Comment on the morphology of the red blood cells.
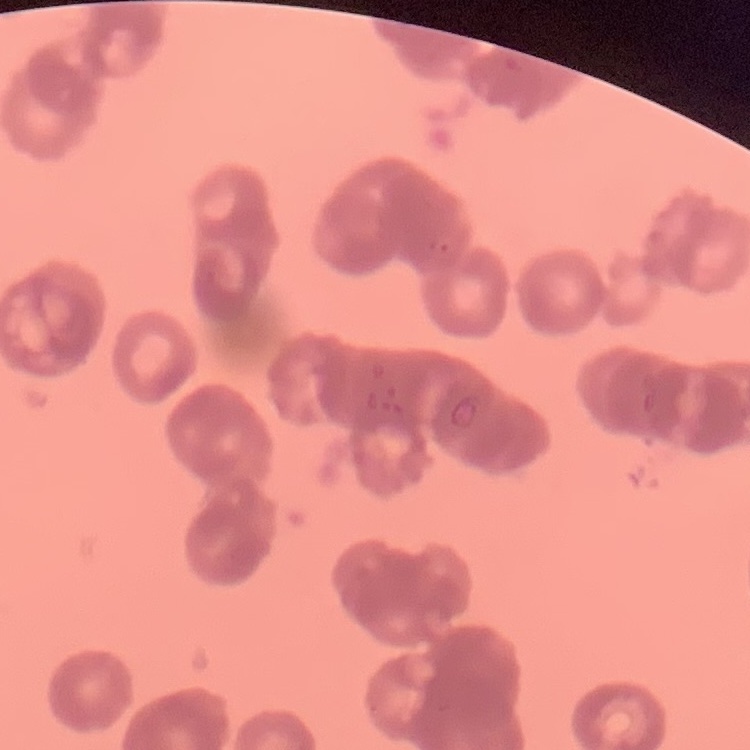
Rouleaux formation.

Summary:
  - Stain: Field's or Giemsa
  - Preparation: thin peripheral smear
  - Image type: one tile cut from a larger photomicrograph